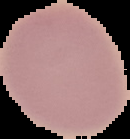

preparation = thin blood smear
result = no malaria parasites detected
image type = segmented cell region with the area outside set to black
image size = 130×139 pixels